Describe the morphology of the erythrocytes.
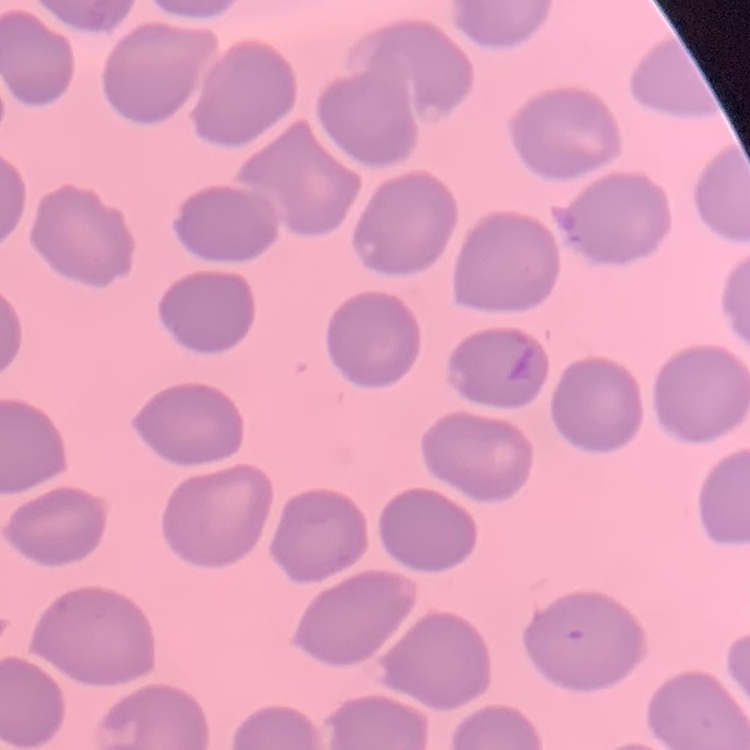

They show no rouleaux formation.

preparation = thin blood smear
stain = Field's or Giemsa
image type = square crop of a larger photomicrograph